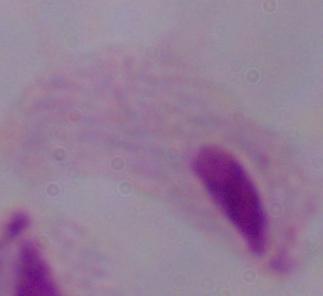 Micrograph. A trichomonad is seen. Captured at 1000x magnification.